Evaluate for malaria.
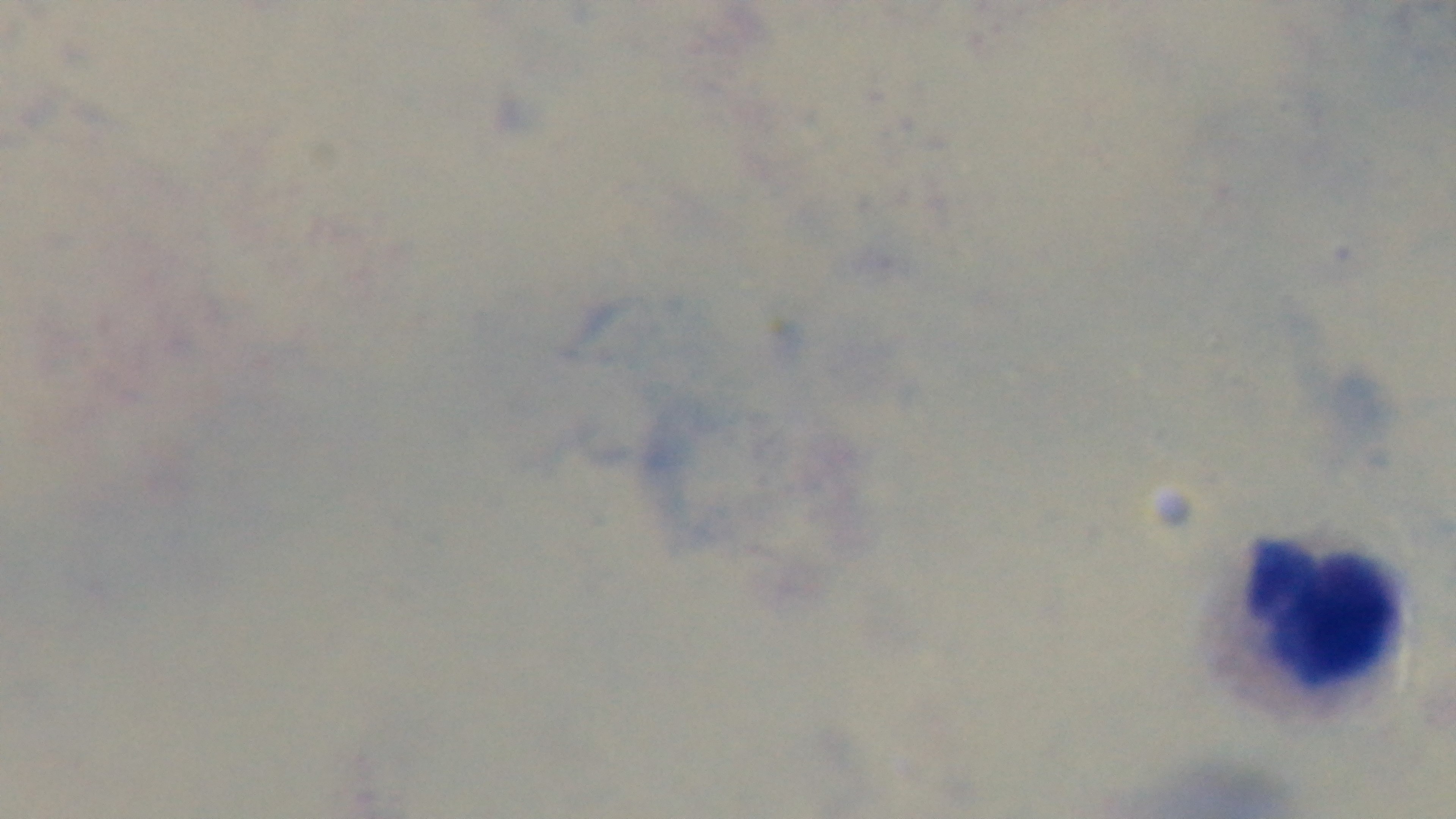
Negative.

field of view = single
preparation = thick
capture = mounted 4K digital camera
modality = light microscopy
objective = 100x oil immersion
stain = Giemsa